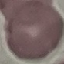
result: no malaria parasites seen
preparation: thin blood film
image_type: cell patch, automatically extracted from a larger field of view and resized to 64 × 64 pixels
capture: smartphone through the microscope eyepiece
stain: Giemsa